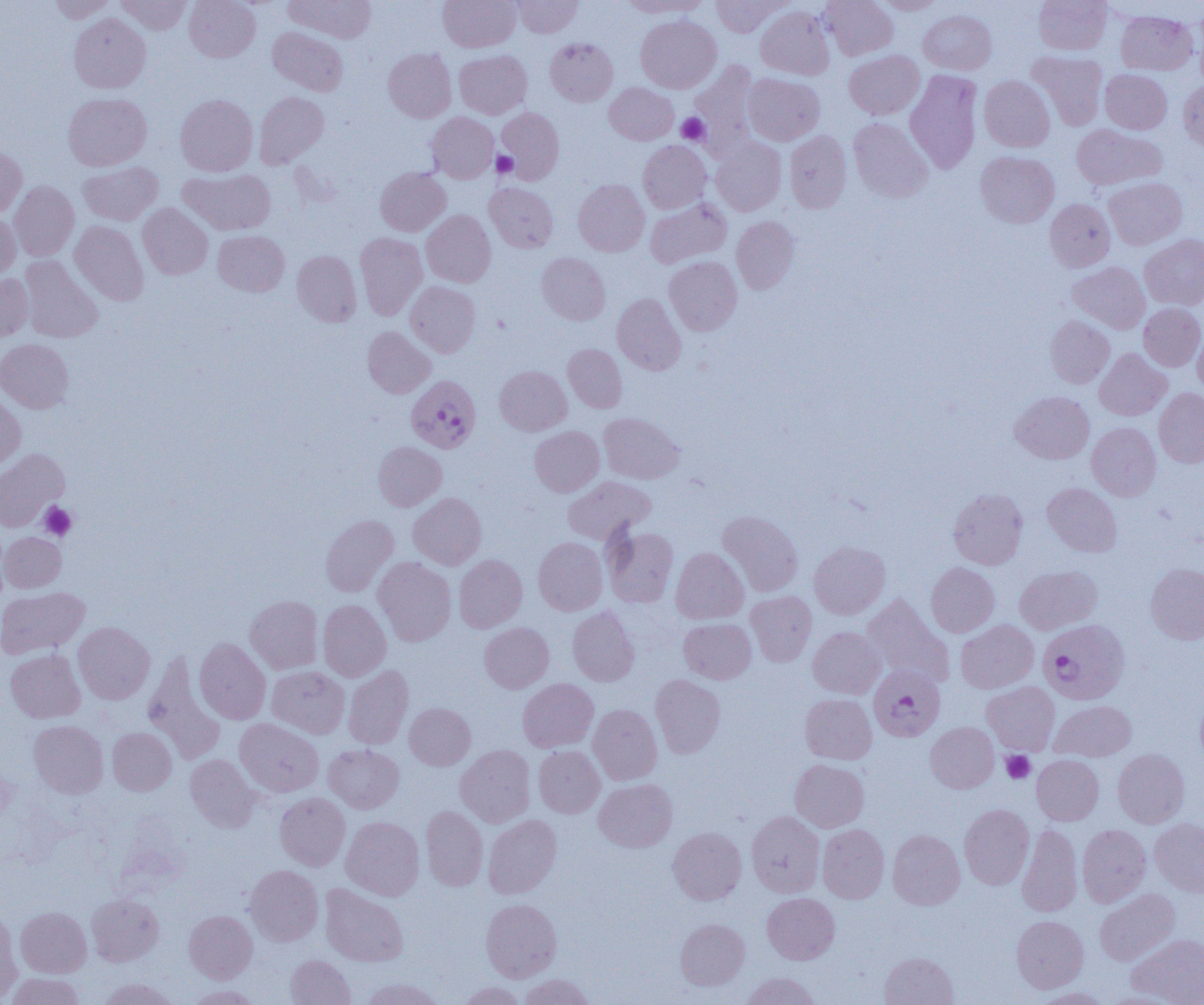

Approximate bounding boxes as named x1/y1/x2/y2 corners in pixels. Plasmodium falciparum-infected red blood cell locations: (x1=406, y1=375, x2=482, y2=453), (x1=1038, y1=619, x2=1130, y2=704), (x1=868, y1=665, x2=945, y2=741). Uninfected red blood cell locations: (x1=48, y1=0, x2=118, y2=23), (x1=116, y1=0, x2=192, y2=34), (x1=184, y1=0, x2=260, y2=62), (x1=284, y1=0, x2=376, y2=42), (x1=438, y1=0, x2=519, y2=52), (x1=511, y1=0, x2=582, y2=37), (x1=620, y1=0, x2=710, y2=17), (x1=711, y1=0, x2=791, y2=37), (x1=820, y1=0, x2=898, y2=60), (x1=874, y1=0, x2=947, y2=15), (x1=1034, y1=0, x2=1112, y2=55), (x1=755, y1=5, x2=834, y2=80), (x1=1193, y1=6, x2=1204, y2=85), (x1=918, y1=10, x2=997, y2=74), (x1=1115, y1=10, x2=1197, y2=75), (x1=69, y1=13, x2=151, y2=93), (x1=636, y1=15, x2=721, y2=93), (x1=268, y1=26, x2=348, y2=96), (x1=545, y1=38, x2=618, y2=106), (x1=383, y1=48, x2=456, y2=123), (x1=454, y1=50, x2=532, y2=119), (x1=844, y1=50, x2=924, y2=119), (x1=1027, y1=51, x2=1108, y2=130), (x1=690, y1=60, x2=761, y2=157), (x1=1100, y1=69, x2=1172, y2=134), (x1=905, y1=70, x2=983, y2=174), (x1=743, y1=73, x2=824, y2=145), (x1=979, y1=76, x2=1055, y2=152), (x1=1179, y1=79, x2=1204, y2=152), (x1=605, y1=82, x2=679, y2=145), (x1=254, y1=91, x2=329, y2=168), (x1=64, y1=93, x2=151, y2=170), (x1=175, y1=94, x2=258, y2=176), (x1=496, y1=107, x2=564, y2=183), (x1=427, y1=113, x2=498, y2=183), (x1=848, y1=117, x2=933, y2=203), (x1=1071, y1=124, x2=1167, y2=190), (x1=785, y1=131, x2=851, y2=213), (x1=711, y1=137, x2=786, y2=215), (x1=638, y1=140, x2=711, y2=213), (x1=0, y1=147, x2=27, y2=217), (x1=975, y1=151, x2=1059, y2=228), (x1=78, y1=161, x2=162, y2=225), (x1=375, y1=167, x2=450, y2=236), (x1=178, y1=169, x2=276, y2=235), (x1=1104, y1=177, x2=1187, y2=250), (x1=573, y1=179, x2=649, y2=256), (x1=9, y1=180, x2=79, y2=261), (x1=484, y1=182, x2=558, y2=252), (x1=645, y1=198, x2=731, y2=268), (x1=1044, y1=198, x2=1115, y2=272), (x1=138, y1=203, x2=213, y2=279), (x1=421, y1=210, x2=496, y2=287), (x1=0, y1=212, x2=20, y2=281), (x1=731, y1=216, x2=799, y2=294), (x1=70, y1=221, x2=148, y2=305), (x1=213, y1=230, x2=289, y2=296), (x1=355, y1=232, x2=427, y2=319), (x1=1139, y1=234, x2=1204, y2=310), (x1=292, y1=250, x2=362, y2=327), (x1=536, y1=252, x2=610, y2=325), (x1=19, y1=255, x2=103, y2=343), (x1=664, y1=256, x2=742, y2=335), (x1=1067, y1=262, x2=1150, y2=333), (x1=0, y1=273, x2=33, y2=341), (x1=406, y1=281, x2=481, y2=357), (x1=612, y1=294, x2=686, y2=375), (x1=1138, y1=303, x2=1204, y2=371), (x1=1045, y1=316, x2=1114, y2=388), (x1=363, y1=326, x2=435, y2=398), (x1=1193, y1=327, x2=1204, y2=396), (x1=0, y1=338, x2=74, y2=413), (x1=563, y1=344, x2=627, y2=413), (x1=1094, y1=348, x2=1170, y2=420), (x1=494, y1=365, x2=571, y2=435), (x1=1154, y1=388, x2=1204, y2=467), (x1=0, y1=391, x2=26, y2=469), (x1=1010, y1=391, x2=1094, y2=463), (x1=598, y1=412, x2=684, y2=484), (x1=1087, y1=422, x2=1161, y2=501), (x1=529, y1=426, x2=604, y2=496), (x1=373, y1=441, x2=447, y2=510), (x1=0, y1=449, x2=69, y2=531), (x1=563, y1=476, x2=655, y2=544), (x1=1043, y1=483, x2=1122, y2=557), (x1=948, y1=488, x2=1027, y2=569), (x1=408, y1=493, x2=487, y2=570), (x1=718, y1=510, x2=803, y2=596), (x1=320, y1=514, x2=399, y2=597), (x1=602, y1=524, x2=679, y2=608), (x1=0, y1=532, x2=66, y2=592), (x1=533, y1=537, x2=608, y2=615), (x1=809, y1=540, x2=890, y2=618), (x1=671, y1=547, x2=748, y2=624), (x1=454, y1=554, x2=527, y2=632), (x1=373, y1=557, x2=456, y2=645), (x1=926, y1=562, x2=999, y2=637), (x1=1146, y1=563, x2=1204, y2=644), (x1=1014, y1=565, x2=1102, y2=635), (x1=0, y1=587, x2=89, y2=659), (x1=746, y1=591, x2=816, y2=666), (x1=862, y1=593, x2=953, y2=686), (x1=246, y1=595, x2=323, y2=674), (x1=318, y1=599, x2=391, y2=681), (x1=567, y1=606, x2=639, y2=686), (x1=679, y1=618, x2=756, y2=684), (x1=955, y1=620, x2=1038, y2=693), (x1=74, y1=622, x2=155, y2=704), (x1=480, y1=622, x2=554, y2=693), (x1=808, y1=626, x2=885, y2=698), (x1=194, y1=638, x2=271, y2=724), (x1=5, y1=649, x2=85, y2=723), (x1=143, y1=652, x2=226, y2=764), (x1=343, y1=665, x2=414, y2=749), (x1=267, y1=666, x2=349, y2=738), (x1=650, y1=674, x2=725, y2=758), (x1=518, y1=678, x2=599, y2=752), (x1=982, y1=681, x2=1059, y2=755), (x1=800, y1=693, x2=877, y2=764), (x1=1195, y1=694, x2=1204, y2=767), (x1=1050, y1=700, x2=1136, y2=762), (x1=404, y1=702, x2=475, y2=770), (x1=588, y1=704, x2=662, y2=784), (x1=234, y1=719, x2=324, y2=797), (x1=29, y1=720, x2=109, y2=798), (x1=926, y1=722, x2=999, y2=792), (x1=107, y1=727, x2=176, y2=795), (x1=323, y1=744, x2=404, y2=813), (x1=456, y1=745, x2=535, y2=827), (x1=534, y1=746, x2=605, y2=818), (x1=1113, y1=749, x2=1190, y2=828), (x1=185, y1=754, x2=261, y2=832), (x1=1032, y1=755, x2=1104, y2=825), (x1=790, y1=759, x2=869, y2=832), (x1=594, y1=778, x2=677, y2=852), (x1=274, y1=792, x2=350, y2=871), (x1=959, y1=804, x2=1034, y2=889), (x1=421, y1=806, x2=488, y2=891), (x1=747, y1=810, x2=825, y2=898), (x1=483, y1=815, x2=561, y2=899), (x1=341, y1=816, x2=424, y2=900), (x1=1149, y1=819, x2=1204, y2=896), (x1=1017, y1=823, x2=1082, y2=917), (x1=817, y1=824, x2=889, y2=903), (x1=1077, y1=824, x2=1151, y2=906), (x1=667, y1=827, x2=746, y2=904), (x1=888, y1=830, x2=965, y2=910), (x1=245, y1=864, x2=324, y2=946), (x1=320, y1=884, x2=408, y2=967), (x1=1094, y1=889, x2=1180, y2=966), (x1=87, y1=892, x2=164, y2=966), (x1=762, y1=893, x2=839, y2=964), (x1=481, y1=899, x2=562, y2=982), (x1=16, y1=907, x2=92, y2=978), (x1=0, y1=909, x2=21, y2=1004), (x1=184, y1=910, x2=258, y2=983), (x1=1011, y1=915, x2=1088, y2=993), (x1=675, y1=919, x2=750, y2=990), (x1=1127, y1=933, x2=1204, y2=1004), (x1=879, y1=952, x2=958, y2=1005), (x1=285, y1=955, x2=355, y2=1005), (x1=741, y1=972, x2=821, y2=1005), (x1=4, y1=973, x2=86, y2=1005), (x1=519, y1=973, x2=595, y2=1005), (x1=360, y1=977, x2=446, y2=1005), (x1=98, y1=978, x2=178, y2=1005), (x1=457, y1=981, x2=527, y2=1005), (x1=184, y1=984, x2=262, y2=1004), (x1=1032, y1=987, x2=1112, y2=1005). Platelet locations: (x1=677, y1=113, x2=709, y2=144), (x1=492, y1=151, x2=518, y2=178), (x1=39, y1=501, x2=77, y2=541), (x1=1001, y1=750, x2=1036, y2=783). Slide-level diagnosis: Plasmodium falciparum. Captured at 1000x magnification. Image is 1204×1005 pixels. Single field of view. Light microscopy. Thin blood film.